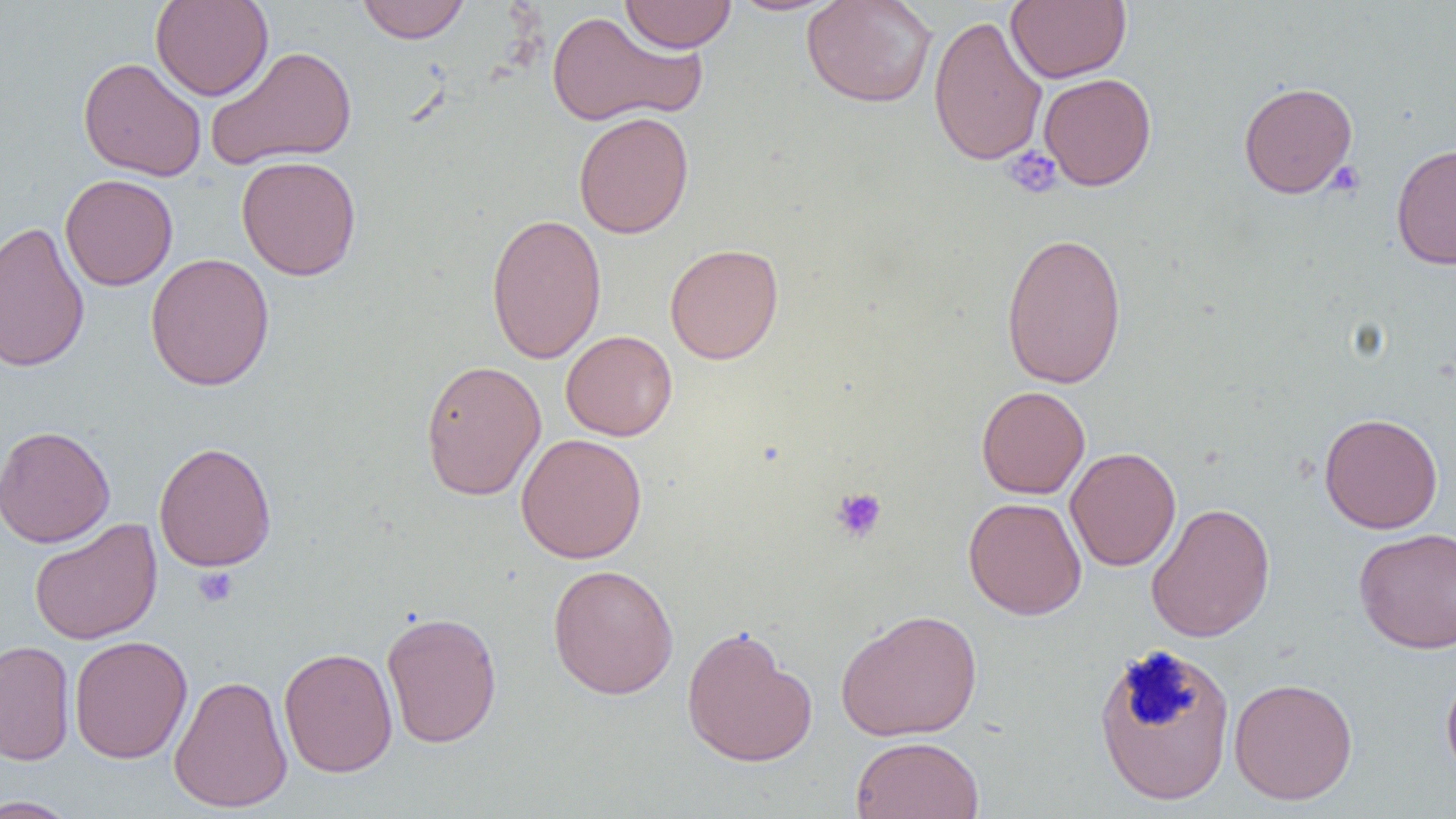
Summary:
  - Coordinate format: approximate bounding boxes as [x1, y1, x2, y2] in pixels
  - Platelet locations: [1003, 146, 1063, 199], [1325, 161, 1366, 198], [830, 487, 888, 543], [193, 565, 239, 607]
  - Uninfected red blood cell locations: [150, 0, 274, 101], [355, 0, 471, 44], [619, 0, 737, 53], [727, 0, 843, 16], [801, 0, 937, 108], [1005, 0, 1132, 83], [545, 10, 706, 128], [928, 14, 1048, 166], [205, 45, 357, 170], [78, 57, 207, 181], [1039, 73, 1156, 191], [1238, 81, 1358, 199], [573, 111, 694, 239], [1390, 142, 1456, 270], [236, 155, 362, 281], [60, 174, 178, 290], [485, 212, 607, 364], [0, 220, 91, 373], [1000, 231, 1128, 390], [664, 243, 784, 364], [145, 252, 275, 391], [561, 330, 677, 441], [420, 359, 546, 500], [976, 385, 1091, 499], [1318, 412, 1444, 534], [0, 425, 115, 548], [515, 433, 647, 563], [153, 441, 277, 572], [1065, 446, 1181, 572], [963, 497, 1087, 620], [1145, 502, 1275, 643], [29, 518, 163, 645], [1353, 526, 1456, 654], [547, 564, 679, 699], [834, 608, 983, 741], [381, 610, 502, 748], [681, 624, 818, 768], [69, 635, 192, 764], [0, 640, 75, 766], [1093, 641, 1235, 806], [278, 646, 398, 777], [1441, 665, 1456, 788], [168, 674, 293, 813], [1228, 677, 1358, 804], [850, 735, 984, 818], [0, 795, 81, 818]
  - Slide-level diagnosis: no evidence of blood parasites
  - Modality: light microscopy
  - Preparation: thin blood smear
  - Image size: 1456×819 pixels
  - Magnification: 1000x
  - Field of view: single